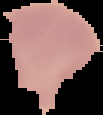 Result: no malaria parasites detected. Segmented cell region on a black background. From a thin blood film. Image is 103×115 pixels.